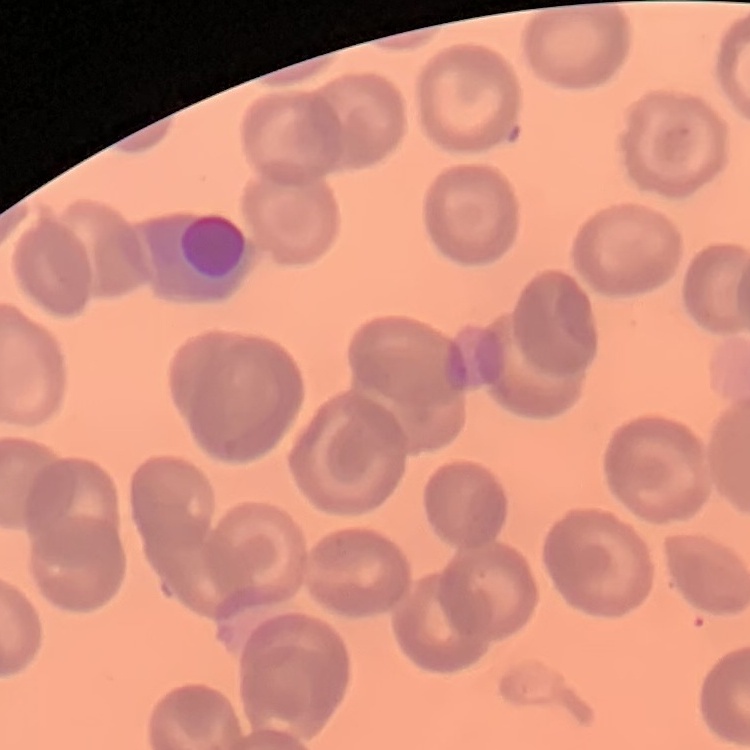

Summary:
  - Erythrocyte morphology: no rouleaux formation
  - Preparation: thin blood smear
  - Image type: one tile cut from a larger photomicrograph
  - Stain: Field's or Giemsa